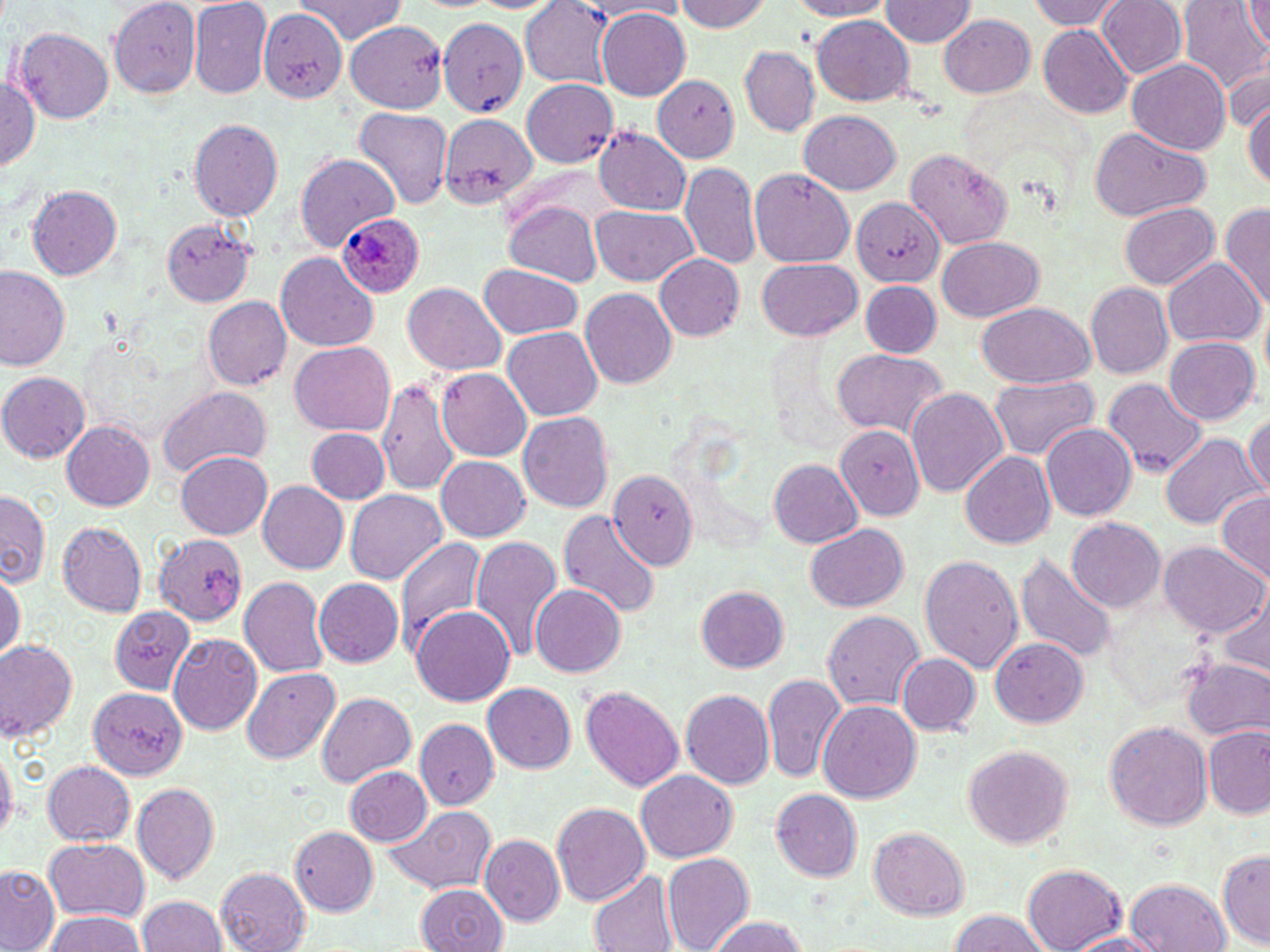
{
  "slide_level_diagnosis": "Plasmodium ovale",
  "field_of_view": "one of a larger specimen",
  "preparation": "thin blood smear",
  "plasmodium_ovale_infected_red_blood_cell_locations": "approximate bounding boxes as (x1, y1, x2, y2) in pixels: (335, 211, 424, 299)",
  "image_size": "1270×952 pixels",
  "magnification": "1000x",
  "stain": "May-Grünwald-Giemsa",
  "uninfected_red_blood_cell_locations": "approximate bounding boxes as (x1, y1, x2, y2) in pixels: (111, 0, 200, 103), (292, 0, 411, 45), (588, 0, 698, 19), (672, 0, 776, 33), (782, 0, 894, 20), (1029, 0, 1122, 31), (1095, 0, 1186, 81), (1179, 0, 1270, 99), (1244, 0, 1269, 49), (880, 1, 977, 47), (189, 2, 270, 99), (520, 2, 614, 88), (260, 8, 347, 102), (596, 8, 690, 101), (939, 13, 1036, 99), (811, 14, 915, 106), (439, 17, 529, 113), (347, 18, 450, 111), (1039, 26, 1134, 119), (15, 28, 114, 121), (740, 46, 820, 136), (1128, 60, 1230, 157), (1228, 61, 1270, 129), (1, 70, 42, 180), (652, 73, 741, 162), (520, 79, 619, 169), (1242, 90, 1270, 196), (352, 106, 454, 211), (798, 110, 901, 194), (443, 114, 542, 209), (190, 118, 282, 223), (1087, 127, 1212, 220), (593, 129, 692, 218), (904, 147, 1013, 250), (293, 154, 399, 251), (681, 163, 762, 273), (750, 168, 856, 268), (26, 185, 122, 282), (852, 197, 942, 287), (503, 200, 603, 286), (1119, 202, 1220, 291), (1221, 202, 1270, 309), (592, 204, 697, 287), (162, 219, 255, 306), (935, 237, 1042, 322), (275, 251, 377, 349), (655, 254, 748, 340), (1164, 257, 1264, 347), (758, 260, 861, 340), (480, 264, 584, 339), (1, 267, 68, 371), (860, 282, 941, 357), (403, 283, 505, 378), (1085, 284, 1173, 377), (580, 289, 677, 390), (202, 296, 292, 392), (976, 302, 1096, 388), (503, 326, 603, 421), (1162, 336, 1259, 426), (290, 344, 395, 434), (829, 348, 950, 445), (437, 367, 532, 460), (376, 371, 463, 501), (1, 372, 89, 463), (989, 376, 1098, 462), (1103, 378, 1209, 478), (156, 385, 271, 477), (906, 387, 1008, 498), (1247, 410, 1270, 499), (517, 413, 614, 513), (61, 420, 154, 511), (1041, 422, 1135, 523), (834, 426, 925, 518), (306, 427, 388, 505), (1163, 436, 1261, 532), (960, 450, 1056, 551), (177, 452, 271, 539), (436, 456, 531, 541), (767, 459, 863, 549), (610, 473, 696, 566), (258, 482, 348, 573), (346, 489, 449, 586), (0, 491, 50, 591), (1215, 491, 1270, 581), (559, 507, 662, 623), (1067, 518, 1166, 613), (58, 520, 147, 618), (803, 523, 910, 614), (153, 535, 245, 627), (470, 535, 564, 666), (393, 538, 486, 658), (1161, 543, 1267, 636), (1016, 551, 1118, 663), (920, 552, 1022, 672), (0, 568, 24, 666), (240, 576, 328, 678), (313, 578, 404, 669), (531, 584, 625, 678), (695, 585, 789, 673), (1212, 588, 1269, 676), (107, 603, 194, 692), (412, 604, 515, 707), (822, 610, 926, 711), (168, 633, 262, 735), (990, 638, 1088, 729), (0, 641, 78, 744), (898, 653, 981, 736), (1181, 658, 1269, 740), (240, 667, 340, 764), (764, 672, 846, 785), (84, 682, 190, 780), (484, 683, 576, 774), (578, 685, 687, 796), (680, 688, 775, 791), (317, 694, 416, 785), (818, 701, 923, 806), (416, 717, 498, 810), (412, 718, 497, 811), (1105, 720, 1211, 829), (1204, 727, 1270, 818), (962, 744, 1074, 852), (0, 745, 16, 844), (41, 760, 135, 847), (344, 767, 434, 848), (636, 771, 738, 861), (134, 782, 220, 884), (771, 789, 862, 881), (549, 801, 651, 909), (383, 806, 498, 897), (290, 827, 379, 911), (868, 827, 970, 918), (481, 835, 564, 927), (43, 838, 150, 920), (1219, 849, 1270, 950), (661, 853, 754, 952), (1024, 863, 1127, 952), (215, 864, 312, 950), (0, 866, 60, 951), (589, 871, 675, 952), (1124, 878, 1231, 952), (414, 885, 510, 952), (138, 894, 226, 952), (42, 910, 149, 952), (942, 910, 1053, 952), (701, 914, 814, 952), (1060, 930, 1175, 951)",
  "modality": "light microscopy"
}